State which parasite is depicted.
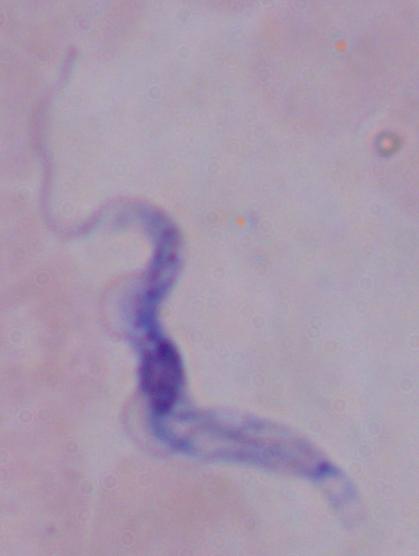

This is a trypanosome.

Photomicrograph. Captured at 1000x magnification.